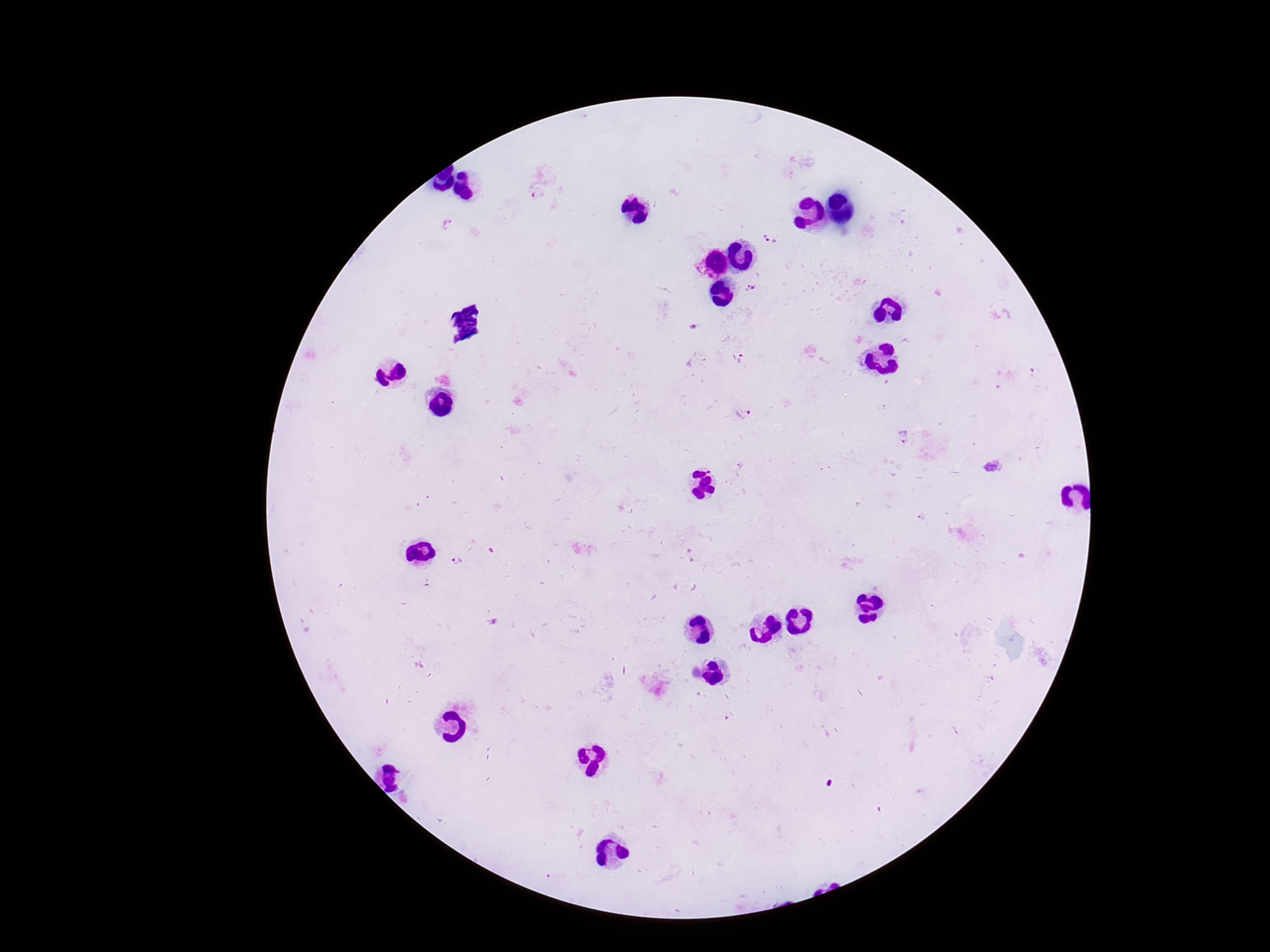
Approximate centers as {x, y} in pixels. Plasmodium parasite locations: {537, 195}, {450, 226}, {772, 238}, {752, 287}, {737, 358}, {743, 415}, {904, 435}, {690, 554}, {460, 563}. One field from this slide. Giemsa stain. Photographed through the microscope eyepiece with a smartphone camera. Thick blood film. Patient malaria status: infected. 100x magnification. Image is 1270×952 pixels.